Name the parasite shown.
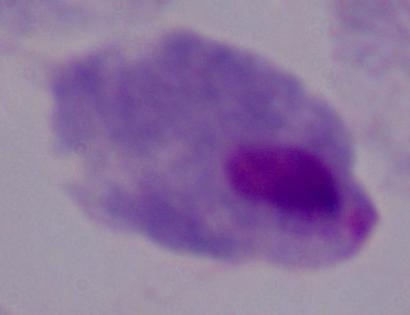
This is a trichomonad.

magnification: 1000x
modality: photomicrograph